Give the preparation type.
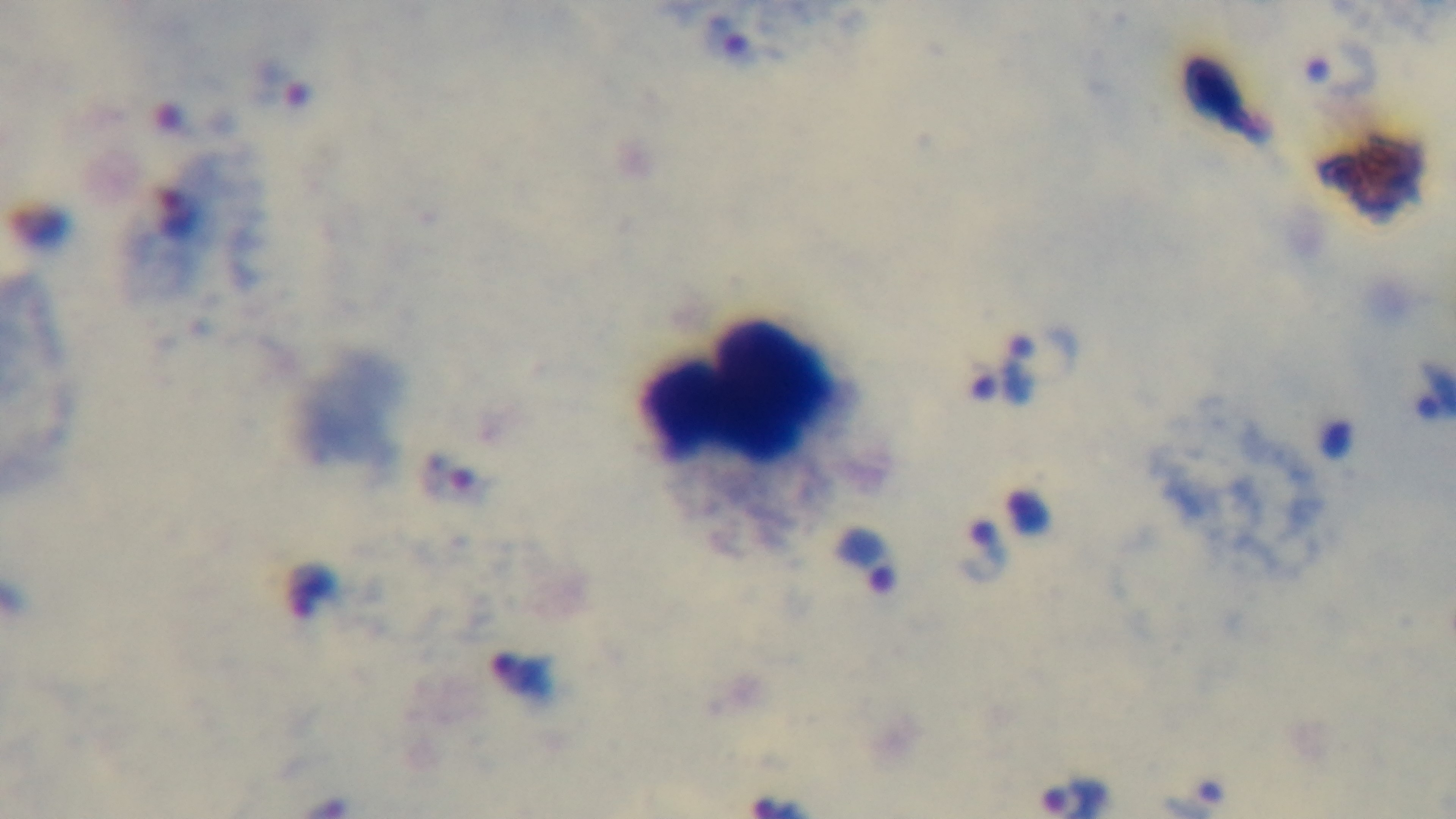

A thick smear.

Mounted 4K digital camera. Malaria status: infected. Giemsa stain. 100x oil-immersion objective. Light microscopy. One field from the slide.